Locate and identify every blood parasite.
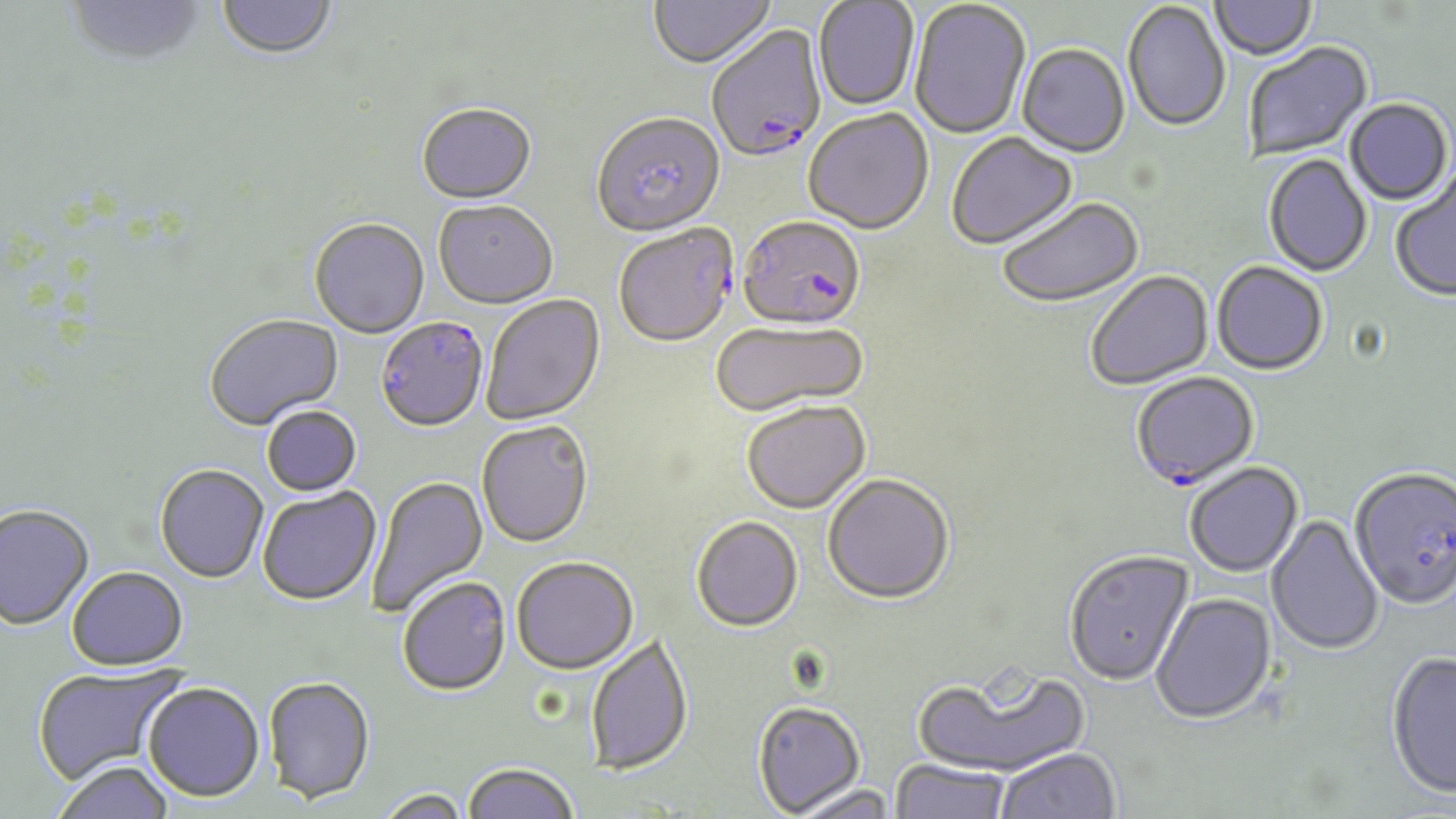
Approximate bounding boxes as [x1, y1, x2, y2] in pixels.
Plasmodium falciparum-infected red blood cells: [705, 26, 827, 166], [737, 219, 866, 334], [614, 226, 738, 350], [375, 318, 489, 435], [1130, 373, 1261, 493], [1349, 470, 1456, 614].
No Plasmodium ovale, Plasmodium malariae, Plasmodium vivax, Babesia divergens, or Trypanosoma brucei observed.

slide-level diagnosis = Plasmodium falciparum
image size = 1456×819 pixels
field of view = one of a larger specimen
magnification = 1000x
stain = May-Grünwald-Giemsa
preparation = thin blood smear
uninfected red blood cell locations = approximate bounding boxes as [x1, y1, x2, y2] in pixels: [65, 0, 207, 70], [216, 0, 338, 62], [649, 0, 776, 73], [1212, 0, 1318, 62], [813, 1, 920, 111], [909, 1, 1031, 141], [1123, 3, 1229, 134], [1244, 43, 1374, 161], [1017, 45, 1130, 159], [1345, 100, 1452, 206], [416, 105, 537, 207], [804, 110, 934, 237], [591, 115, 726, 240], [947, 133, 1079, 252], [1263, 155, 1373, 278], [1390, 167, 1456, 304], [998, 199, 1145, 310], [434, 203, 558, 311], [309, 219, 430, 340], [1212, 263, 1328, 377], [1087, 272, 1214, 390], [481, 295, 607, 427], [205, 315, 344, 432], [709, 322, 869, 420], [742, 404, 870, 516], [262, 407, 362, 499], [476, 423, 594, 550], [1185, 464, 1304, 579], [155, 466, 268, 586], [366, 475, 488, 618], [822, 476, 955, 607], [258, 487, 382, 608], [0, 507, 95, 633], [1265, 515, 1384, 657], [691, 518, 803, 634], [1064, 552, 1195, 689], [512, 560, 639, 677], [67, 569, 188, 674], [398, 579, 511, 698], [1150, 594, 1277, 727], [586, 635, 694, 778], [1385, 653, 1456, 802], [33, 665, 187, 787], [911, 667, 1092, 779], [263, 679, 375, 807], [142, 684, 265, 805], [752, 702, 865, 817], [997, 750, 1121, 819], [889, 761, 1011, 819], [53, 763, 174, 819], [463, 763, 578, 819], [789, 785, 899, 819], [373, 790, 473, 819]
modality = light microscopy